State the preparation type.
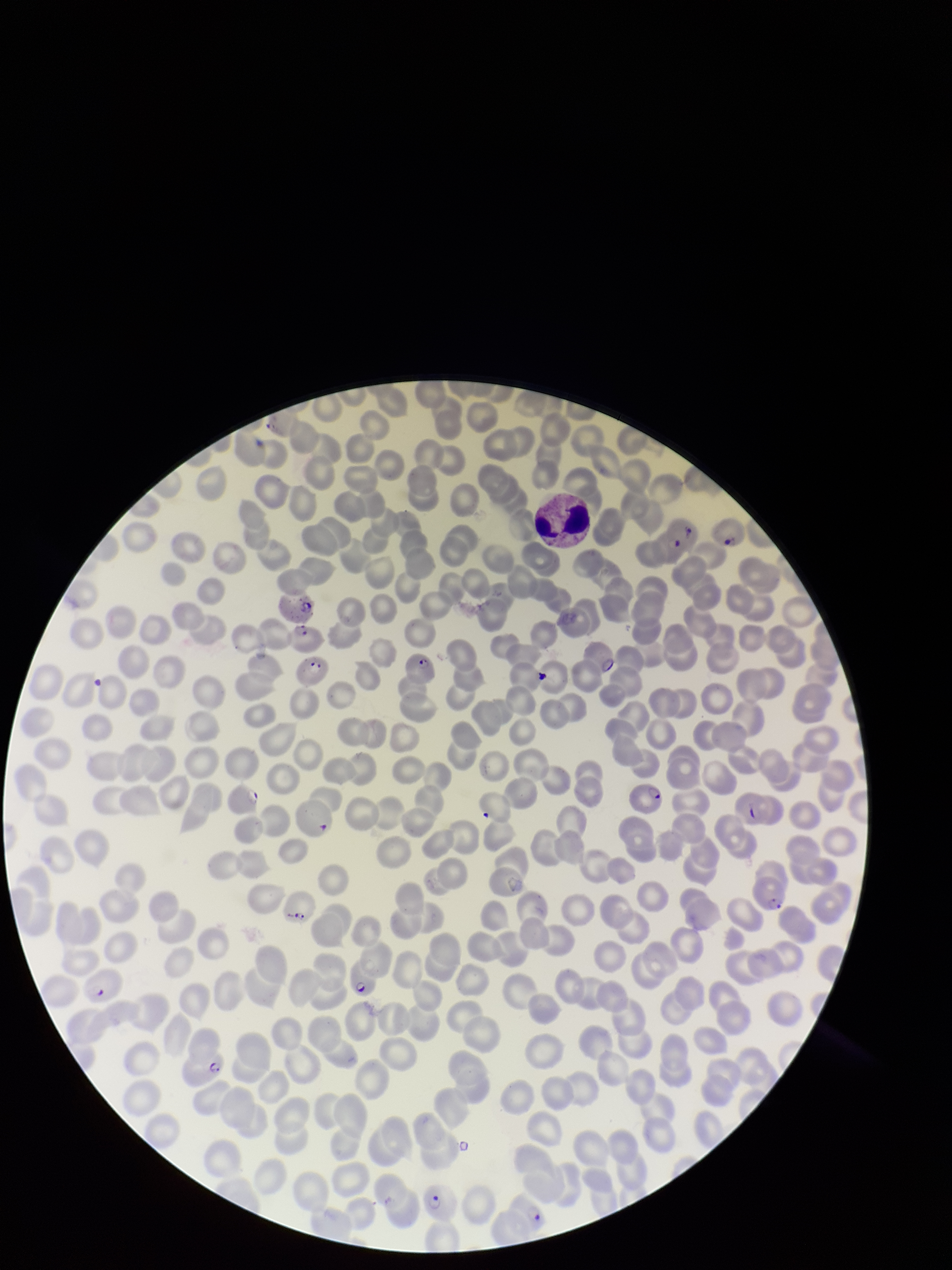
It is a thin blood smear.

Summary:
  - Patient malaria status: infected
  - Image size: 952×1270 pixels
  - Stain: Giemsa
  - Red blood cell count: 200
  - Species reported for this patient: Plasmodium falciparum
  - Parasitized red blood cells: detected
  - Parasitized red blood cell count: 18
  - Capture: smartphone photograph through the microscope eyepiece
  - Field of view: one from this slide